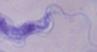

Summary:
  - Identification: trypanosome
  - Modality: photomicrograph
  - Magnification: 1000x